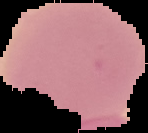
Cell region segmented out of the field of view; the surrounding area is masked to black. Image is 148×133 pixels. Malaria status: uninfected. From a thin blood smear.